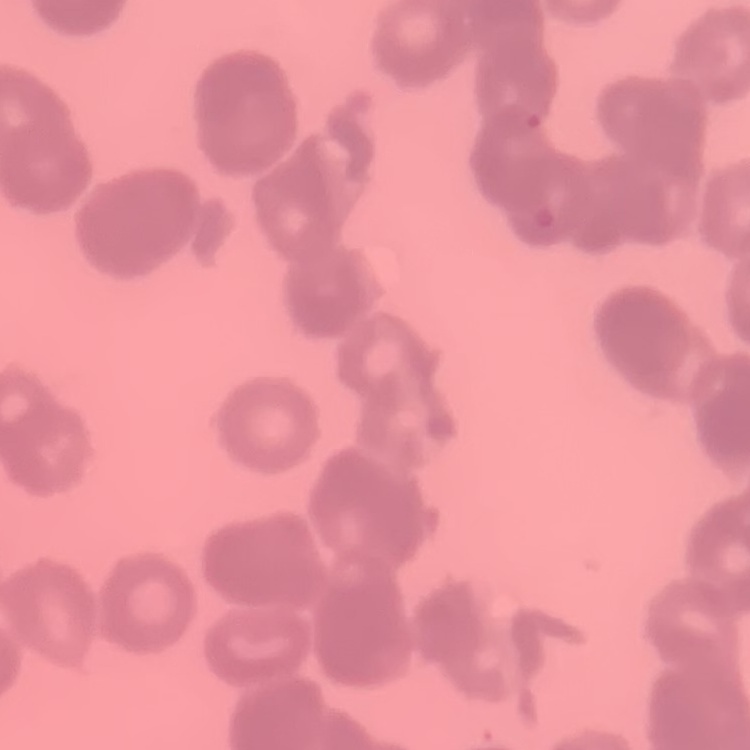

The red blood cells exhibit rouleaux formation. Thin peripheral smear. Square crop of a larger photomicrograph. Field's or Giemsa stain.